Report the malaria status of this cell.
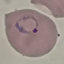
Parasitized.

Summary:
  - Image type: automatically extracted cell patch, resized to 64 × 64 pixels
  - Stain: Giemsa
  - Capture: smartphone through the microscope eyepiece
  - Preparation: thin smear